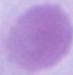

Summary:
  - Modality: photomicrograph
  - Identification: erythrocyte
  - Magnification: 1000x